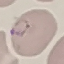

Malaria status: parasitized. Thin blood film. Giemsa stain. Photographed with a smartphone camera at the microscope eyepiece. Cell patch, automatically extracted from a larger field of view and resized to 64 × 64 pixels.